Report the malaria status of this cell.
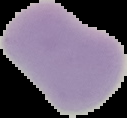

It is uninfected.

Image is 127×118 pixels. From a thin blood film. Cell region segmented out of the field of view; the surrounding area is masked to black.